Outline each Plasmodium vivax-infected red blood cell.
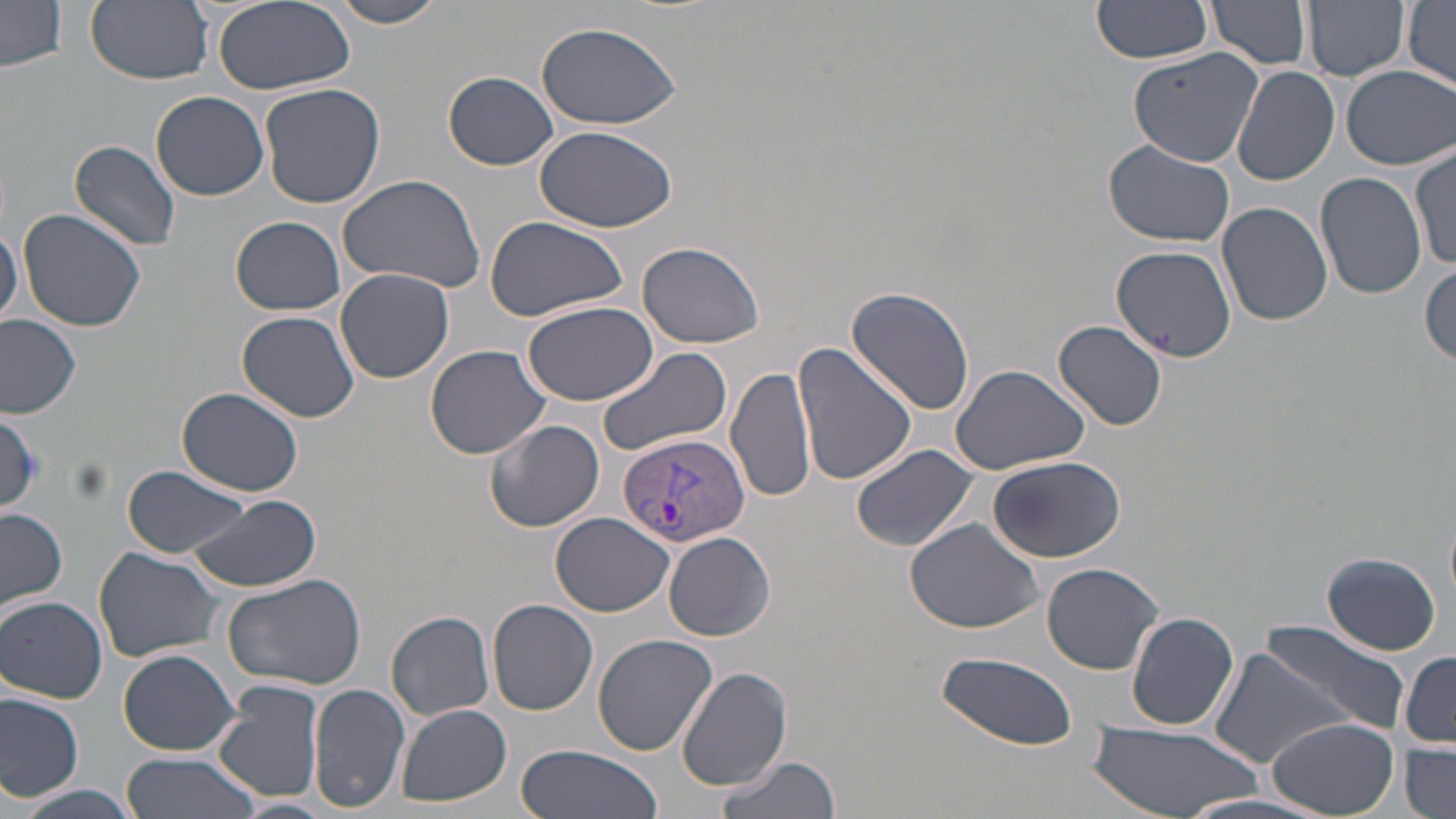

Approximate bounding boxes as [x1, y1, x2, y2] in pixels.
Plasmodium vivax-infected red blood cells: [619, 433, 751, 548].

Summary:
  - Uninfected red blood cell locations: [86, 0, 214, 86], [212, 0, 354, 95], [326, 0, 451, 28], [1092, 0, 1214, 63], [1207, 0, 1313, 70], [1302, 0, 1411, 82], [1403, 1, 1456, 88], [0, 3, 67, 73], [533, 20, 684, 130], [1128, 46, 1264, 168], [1341, 65, 1454, 168], [1234, 67, 1340, 187], [444, 71, 558, 170], [259, 81, 385, 209], [151, 90, 269, 201], [534, 126, 678, 233], [70, 140, 183, 251], [1101, 140, 1236, 247], [1411, 146, 1455, 271], [337, 171, 486, 294], [1316, 173, 1426, 299], [1218, 201, 1331, 325], [16, 208, 148, 332], [482, 213, 629, 323], [230, 216, 347, 315], [0, 222, 22, 328], [636, 241, 765, 349], [1112, 244, 1237, 361], [1419, 263, 1455, 367], [336, 267, 454, 384], [847, 285, 977, 416], [521, 299, 658, 405], [237, 311, 361, 422], [0, 312, 83, 418], [1055, 320, 1167, 430], [792, 341, 916, 487], [424, 344, 551, 459], [596, 344, 733, 459], [726, 364, 816, 505], [949, 364, 1091, 475], [176, 387, 305, 497], [0, 411, 45, 510], [485, 418, 605, 532], [850, 443, 979, 553], [988, 454, 1127, 563], [124, 465, 257, 560], [188, 493, 321, 593], [1, 509, 68, 613], [552, 512, 674, 616], [904, 518, 1044, 637], [664, 532, 775, 641], [93, 546, 225, 663], [1322, 551, 1442, 656], [1042, 562, 1164, 674], [222, 571, 369, 692], [1, 596, 107, 703], [487, 598, 597, 716], [1127, 611, 1240, 730], [387, 612, 495, 720], [1263, 622, 1407, 732], [592, 633, 718, 756], [1209, 645, 1357, 771], [118, 648, 242, 756], [933, 652, 1080, 747], [1401, 652, 1456, 747], [676, 666, 793, 791], [215, 681, 326, 805], [308, 683, 409, 813], [0, 694, 85, 802], [398, 704, 511, 805], [1268, 716, 1399, 816], [1087, 722, 1263, 818], [1401, 744, 1456, 818], [516, 745, 662, 819], [120, 753, 262, 819], [715, 756, 839, 819], [9, 784, 150, 819], [225, 798, 336, 818]
  - Slide-level diagnosis: Plasmodium vivax
  - Preparation: thin blood smear
  - Magnification: 1000x
  - Field of view: single
  - Image size: 1456×819 pixels
  - Modality: optical microscopy
  - Stain: May-Grünwald-Giemsa